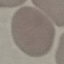

malaria status = uninfected
stain = Giemsa
capture = smartphone camera at the microscope eyepiece
preparation = thin blood smear
image type = cell patch, automatically extracted from a larger field of view and resized to 64 × 64 pixels